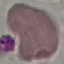

Summary:
  - Malaria status: uninfected
  - Stain: Giemsa
  - Capture: smartphone through the microscope eyepiece
  - Image type: automatically extracted cell patch, resized to 64 × 64 pixels
  - Preparation: thin blood film